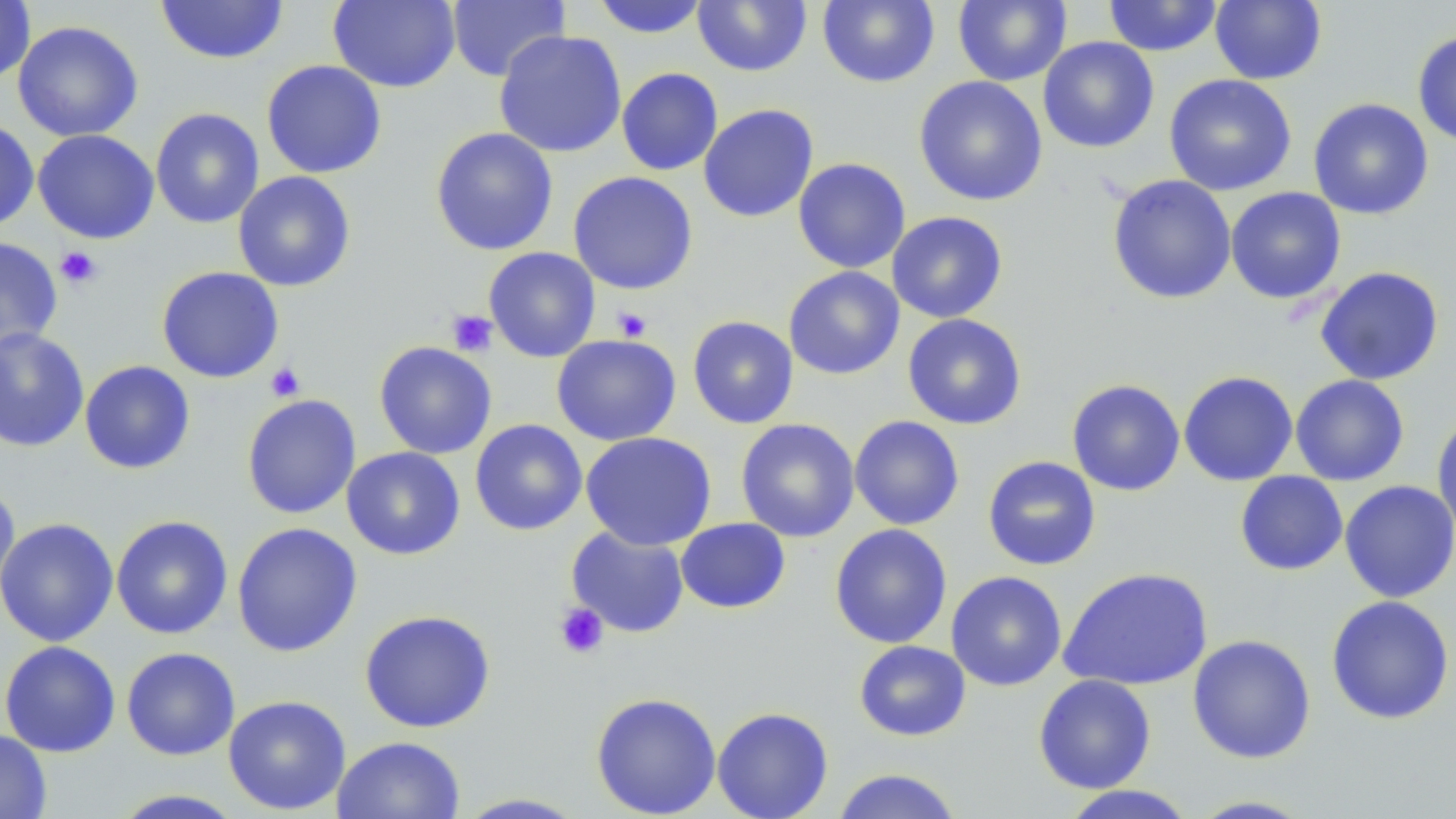

{
  "slide_level_diagnosis": "no evidence of blood parasites",
  "modality": "optical microscopy",
  "field_of_view": "one of a larger specimen",
  "image_size": "1456×819 pixels",
  "platelet_locations": "approximate bounding boxes as (x1, y1, x2, y2) in pixels: (55, 246, 102, 289), (612, 306, 652, 341), (447, 309, 498, 357), (265, 362, 305, 402), (554, 602, 609, 659)",
  "stain": "May-Grünwald-Giemsa",
  "magnification": "1000x",
  "uninfected_red_blood_cell_locations": "approximate bounding boxes as (x1, y1, x2, y2) in pixels: (328, 0, 461, 92), (446, 0, 570, 83), (592, 0, 710, 38), (817, 0, 940, 88), (953, 0, 1071, 86), (1103, 0, 1223, 57), (1210, 0, 1327, 85), (0, 1, 36, 83), (155, 1, 289, 65), (692, 1, 812, 76), (13, 20, 143, 142), (493, 30, 627, 158), (1413, 31, 1456, 148), (1038, 36, 1159, 153), (261, 60, 387, 178), (616, 67, 723, 176), (1164, 74, 1297, 196), (913, 75, 1048, 206), (1308, 98, 1434, 220), (698, 103, 819, 223), (150, 107, 264, 229), (0, 118, 39, 233), (430, 127, 558, 256), (33, 129, 159, 244), (793, 157, 911, 273), (233, 171, 356, 292), (568, 171, 698, 295), (1107, 174, 1237, 304), (1225, 187, 1346, 304), (887, 211, 1008, 323), (0, 237, 62, 353), (484, 247, 600, 362), (156, 266, 284, 383), (783, 266, 905, 380), (1314, 266, 1445, 385), (902, 313, 1027, 430), (688, 316, 799, 429), (0, 327, 90, 452), (551, 334, 681, 446), (374, 341, 497, 459), (79, 360, 196, 474), (1178, 371, 1298, 486), (1290, 374, 1410, 486), (1067, 378, 1186, 496), (241, 394, 361, 519), (1432, 410, 1456, 538), (849, 415, 965, 530), (470, 418, 587, 535), (735, 419, 860, 543), (579, 431, 717, 551), (341, 446, 465, 560), (982, 455, 1101, 571), (1235, 471, 1348, 576), (1339, 480, 1456, 603), (0, 484, 20, 606), (111, 515, 233, 639), (0, 517, 119, 647), (675, 517, 791, 613), (231, 522, 363, 657), (829, 523, 952, 649), (566, 526, 690, 638), (1058, 566, 1213, 690), (945, 571, 1067, 691), (1326, 595, 1455, 724), (359, 610, 496, 733), (1186, 634, 1316, 764), (853, 640, 971, 741), (0, 641, 121, 757), (121, 647, 240, 760), (1033, 674, 1157, 794), (590, 692, 721, 818), (222, 694, 351, 815), (712, 706, 834, 819), (0, 729, 52, 818), (331, 735, 466, 819), (830, 768, 964, 818), (1058, 785, 1198, 819), (109, 789, 247, 818), (453, 793, 591, 818), (1186, 795, 1317, 818)",
  "preparation": "thin blood film"
}